Identify the blood parasite species.
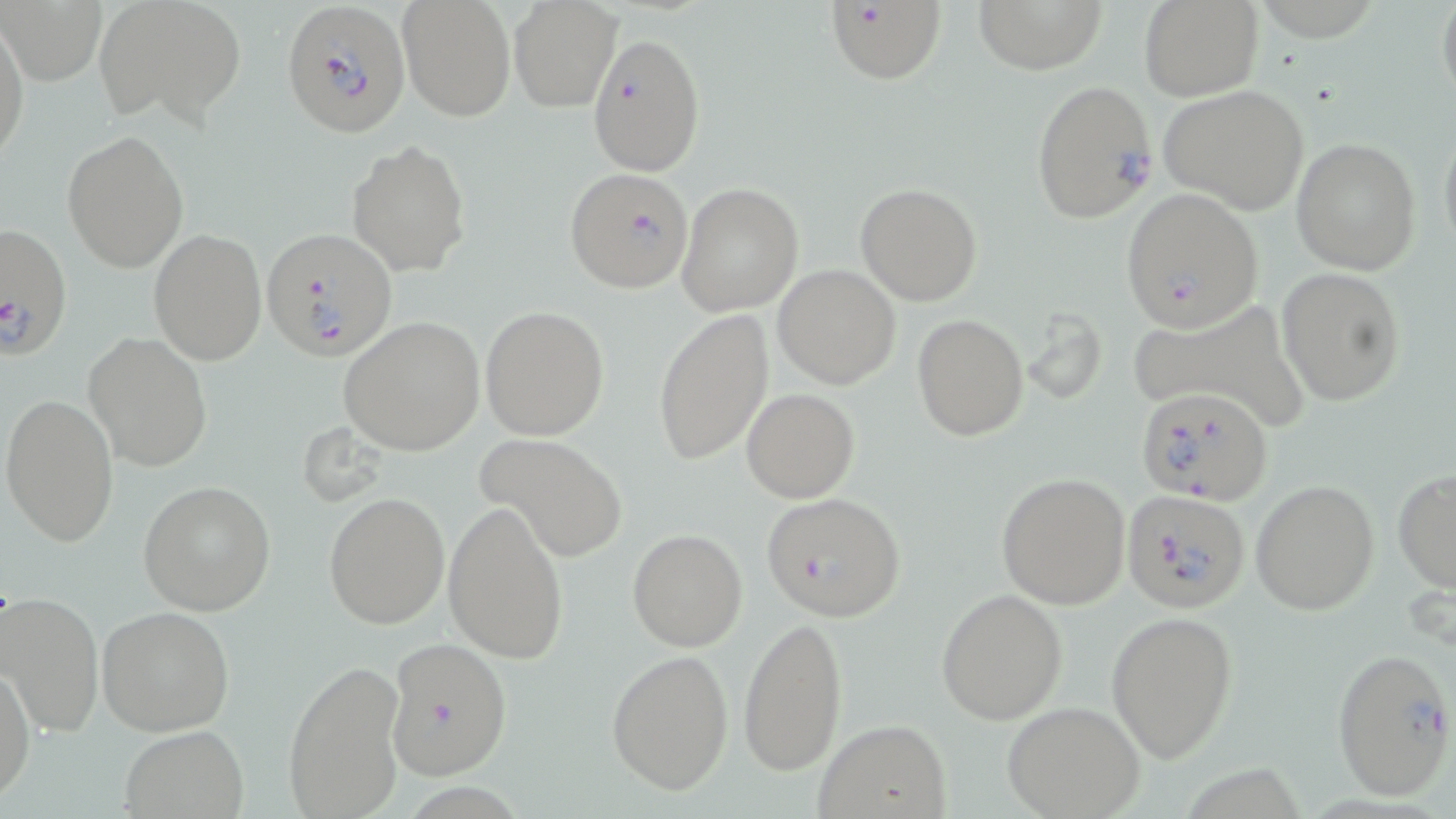
Plasmodium falciparum.

Approximate bounding boxes as (x1, y1, x2, y2) in pixels. Uninfected red blood cell locations: (96, 0, 247, 125), (973, 0, 1109, 73), (1139, 0, 1263, 101), (1437, 0, 1456, 112), (508, 1, 623, 112), (396, 2, 513, 121), (1, 15, 29, 170), (1158, 83, 1310, 215), (1438, 116, 1456, 262), (62, 130, 189, 271), (1291, 137, 1422, 274), (347, 139, 470, 275), (855, 182, 983, 305), (677, 183, 805, 317), (148, 229, 267, 365), (773, 265, 901, 390), (1276, 266, 1405, 406), (1130, 299, 1307, 423), (481, 305, 610, 440), (652, 309, 775, 467), (913, 314, 1028, 441), (339, 316, 485, 454), (82, 331, 213, 472), (741, 388, 859, 501), (1, 393, 121, 548), (476, 432, 627, 562), (1393, 468, 1455, 593), (997, 473, 1131, 610), (139, 480, 277, 615), (1250, 480, 1380, 615), (323, 492, 452, 630), (443, 501, 567, 664), (626, 528, 747, 652), (937, 587, 1069, 724), (2, 592, 104, 738), (96, 606, 235, 737), (1106, 609, 1240, 765), (737, 614, 850, 777), (606, 649, 734, 794), (283, 657, 406, 819), (1, 661, 36, 802), (1001, 701, 1146, 818), (812, 718, 951, 818), (119, 726, 250, 817). Plasmodium falciparum-infected red blood cell locations: (282, 1, 412, 137), (823, 3, 948, 86), (587, 31, 706, 177), (1029, 80, 1159, 222), (564, 165, 695, 296), (1117, 188, 1266, 332), (0, 221, 71, 357), (262, 226, 397, 362), (1137, 385, 1274, 506), (1121, 488, 1251, 613), (761, 492, 906, 621), (384, 636, 513, 780), (1331, 647, 1454, 800). Thin blood film. May-Grünwald-Giemsa-stained preparation. Image is 1456×819 pixels. Single field of view. Light microscopy. Captured at 1000x magnification.